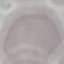 Result: no malaria parasites seen. Acquired by smartphone through the microscope eyepiece. Automatically extracted cell patch, resized to 64 × 64 pixels. Thin blood smear. Giemsa stain.